Locate platelets.
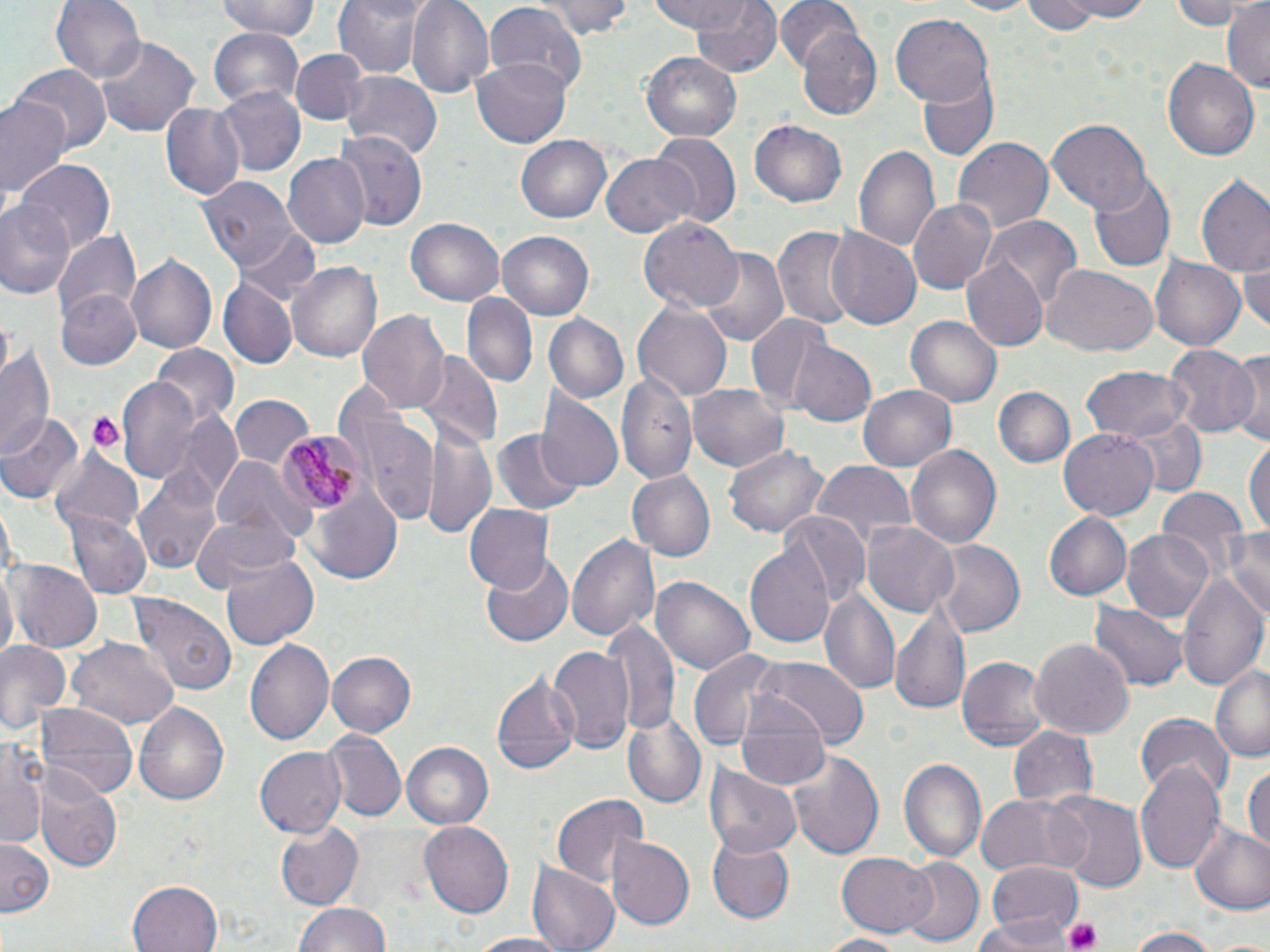

Approximate bounding boxes as [x1, y1, x2, y2] in pixels.
Platelets: [82, 409, 126, 457], [1063, 918, 1103, 952].

Uninfected red blood cell locations: [54, 0, 147, 86], [216, 0, 321, 42], [332, 0, 428, 79], [407, 0, 494, 97], [536, 0, 632, 39], [649, 0, 754, 35], [689, 0, 784, 78], [774, 0, 862, 75], [946, 0, 1041, 16], [1051, 0, 1159, 21], [1170, 0, 1255, 30], [1222, 0, 1270, 90], [1020, 1, 1101, 37], [481, 3, 586, 98], [892, 13, 993, 107], [798, 24, 883, 121], [209, 27, 304, 108], [94, 36, 200, 139], [292, 48, 365, 125], [641, 50, 741, 140], [474, 57, 573, 148], [1162, 57, 1260, 162], [13, 65, 109, 153], [917, 71, 997, 162], [341, 72, 443, 162], [216, 87, 305, 178], [0, 94, 71, 203], [161, 102, 245, 201], [1047, 120, 1150, 212], [750, 121, 847, 208], [335, 129, 427, 232], [517, 135, 611, 223], [650, 135, 740, 227], [953, 137, 1054, 235], [853, 142, 943, 258], [282, 152, 370, 249], [601, 154, 696, 238], [17, 160, 115, 253], [1194, 171, 1270, 279], [198, 175, 299, 272], [1089, 175, 1175, 272], [0, 197, 77, 302], [908, 197, 997, 295], [406, 218, 504, 306], [639, 218, 743, 314], [986, 218, 1082, 312], [773, 226, 857, 331], [235, 227, 323, 303], [826, 228, 921, 332], [54, 229, 140, 333], [498, 232, 592, 320], [697, 248, 790, 347], [1149, 252, 1245, 350], [125, 254, 216, 355], [1239, 255, 1270, 334], [962, 257, 1048, 352], [289, 259, 382, 363], [1042, 265, 1155, 358], [219, 279, 295, 367], [57, 289, 143, 372], [462, 293, 537, 392], [634, 303, 731, 399], [358, 311, 451, 416], [745, 313, 835, 413], [544, 314, 629, 404], [907, 315, 1002, 408], [1, 342, 57, 459], [792, 342, 875, 425], [1164, 345, 1259, 439], [152, 346, 239, 429], [416, 352, 502, 452], [1226, 353, 1269, 444], [1080, 365, 1193, 443], [617, 374, 699, 483], [118, 377, 201, 480], [689, 381, 790, 471], [860, 386, 955, 471], [994, 387, 1077, 469], [230, 394, 316, 473], [536, 397, 622, 493], [353, 407, 437, 527], [1117, 410, 1206, 499], [0, 411, 82, 503], [182, 417, 241, 499], [429, 423, 495, 541], [1058, 428, 1158, 522], [492, 429, 582, 516], [1245, 436, 1270, 542], [905, 444, 1003, 550], [724, 445, 829, 541], [52, 448, 141, 537], [213, 457, 308, 546], [809, 462, 916, 552], [134, 463, 223, 576], [627, 470, 717, 563], [307, 484, 403, 586], [1154, 489, 1250, 583], [466, 503, 554, 594], [63, 508, 152, 599], [1042, 510, 1132, 601], [782, 511, 866, 606], [189, 515, 298, 595], [862, 520, 959, 618], [1220, 529, 1270, 625], [1122, 530, 1213, 624], [565, 531, 660, 644], [744, 540, 837, 652], [932, 540, 1025, 637], [221, 555, 320, 649], [482, 555, 574, 647], [7, 560, 101, 652], [1175, 569, 1267, 690], [652, 575, 756, 675], [821, 587, 901, 697], [131, 597, 237, 698], [892, 601, 973, 719], [1090, 602, 1188, 691], [605, 618, 679, 741], [67, 636, 177, 729], [1030, 636, 1135, 738], [0, 637, 70, 740], [246, 639, 334, 747], [549, 646, 632, 755], [688, 649, 782, 754], [326, 650, 416, 737], [958, 655, 1050, 751], [753, 657, 870, 749], [1212, 659, 1270, 762], [491, 672, 582, 777], [733, 694, 834, 792], [135, 700, 229, 807], [34, 702, 138, 800], [1135, 712, 1232, 800], [624, 718, 705, 805], [1007, 725, 1099, 806], [323, 732, 404, 821], [1, 734, 49, 846], [401, 741, 493, 830], [785, 747, 884, 862], [255, 748, 347, 838], [899, 757, 986, 863], [1136, 759, 1226, 876], [1243, 764, 1270, 851], [704, 765, 802, 859], [37, 772, 122, 872], [550, 792, 649, 890], [974, 793, 1090, 877], [1050, 793, 1147, 893], [420, 821, 513, 919], [278, 822, 364, 910], [1188, 824, 1270, 916], [607, 834, 696, 931], [707, 834, 795, 925], [0, 840, 53, 913], [836, 851, 936, 934], [898, 856, 983, 946], [986, 862, 1081, 945], [527, 864, 619, 952], [128, 880, 224, 952], [293, 901, 390, 952], [975, 919, 1064, 952], [1122, 927, 1221, 952], [460, 933, 574, 951], [816, 933, 911, 951], [1209, 934, 1270, 952]. Plasmodium malariae-infected red blood cell locations: [278, 430, 364, 514]. Slide-level diagnosis: Plasmodium malariae. Image is 1270×952 pixels. Captured at 1000x magnification. Light microscopy. Thin blood film. One field of a larger specimen. May-Grünwald-Giemsa-stained preparation.